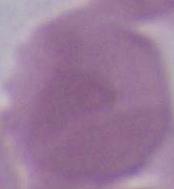

identification = erythrocyte
modality = photomicrograph
magnification = 1000x